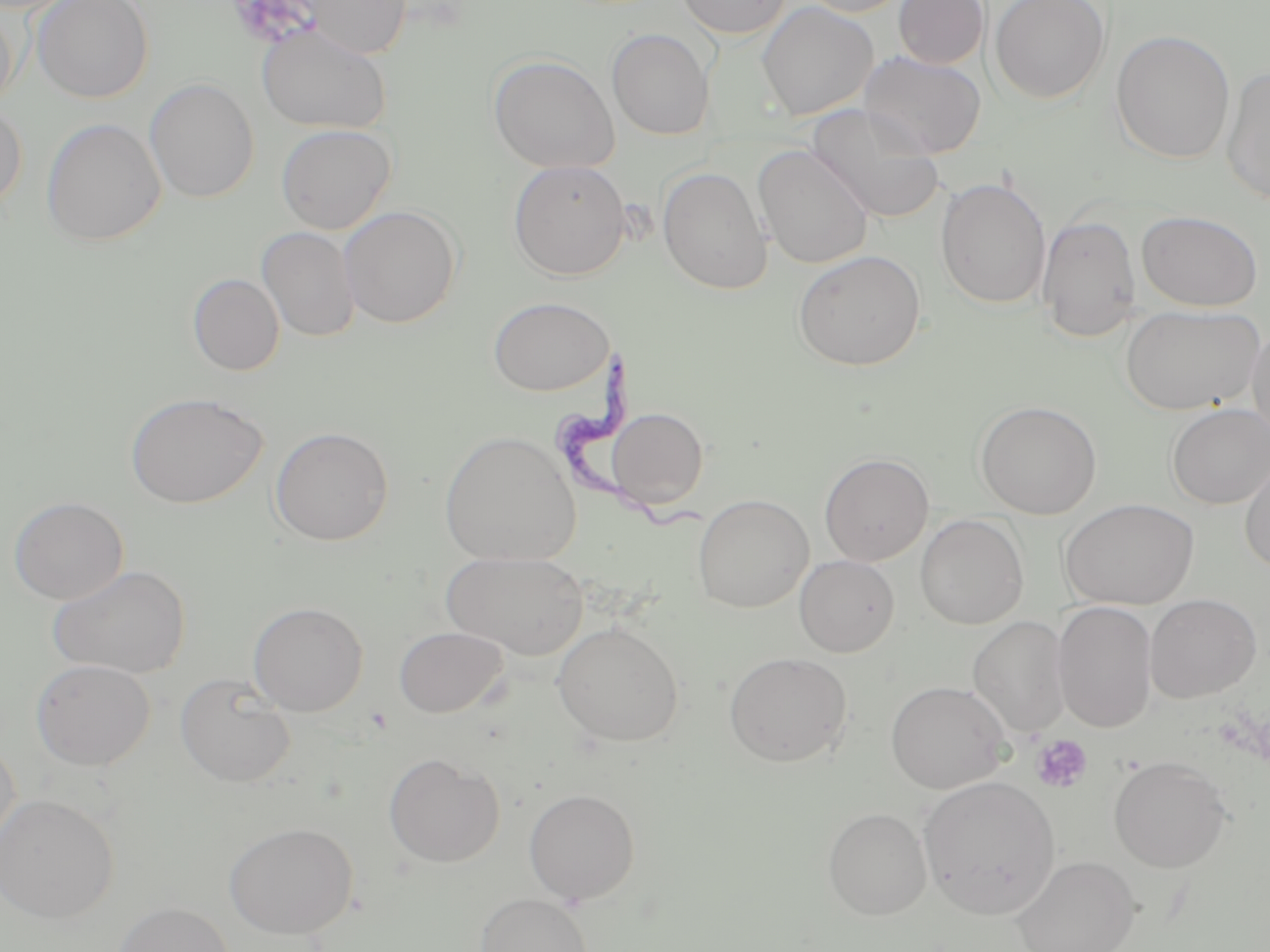
slide-level diagnosis = Trypanosoma brucei
field of view = one of a larger specimen
platelet locations = approximate bounding boxes as (x1, y1, x2, y2) in pixels: (223, 1, 320, 49), (1030, 734, 1093, 793)
image size = 1270×952 pixels
preparation = thin blood smear
stain = May-Grünwald-Giemsa
magnification = 1000x
modality = optical microscopy
Trypanosoma brucei locations = approximate bounding boxes as (x1, y1, x2, y2) in pixels: (555, 350, 704, 530)
uninfected red blood cell locations = approximate bounding boxes as (x1, y1, x2, y2) in pixels: (33, 0, 154, 103), (297, 0, 412, 59), (674, 0, 791, 39), (794, 0, 913, 17), (893, 0, 988, 69), (989, 0, 1111, 104), (756, 2, 878, 120), (0, 4, 19, 113), (257, 24, 390, 134), (607, 28, 715, 140), (1111, 29, 1235, 164), (857, 51, 987, 159), (488, 54, 619, 174), (1221, 67, 1270, 206), (144, 78, 259, 203), (0, 100, 28, 216), (808, 107, 945, 223), (41, 117, 166, 247), (275, 123, 396, 234), (752, 144, 874, 269), (508, 160, 631, 280), (657, 166, 773, 295), (935, 176, 1051, 310), (339, 205, 461, 328), (1137, 210, 1264, 311), (1037, 214, 1142, 342), (257, 226, 360, 342), (793, 250, 926, 371), (187, 273, 285, 376), (487, 296, 614, 396), (1120, 304, 1264, 415), (1247, 322, 1270, 447), (125, 392, 268, 509), (975, 400, 1102, 519), (1166, 403, 1270, 509), (606, 407, 709, 510), (270, 426, 394, 546), (439, 429, 581, 567), (1239, 451, 1270, 576), (819, 453, 934, 565), (692, 493, 814, 613), (9, 496, 129, 604), (1058, 498, 1200, 610), (915, 514, 1029, 630), (442, 550, 589, 659), (794, 555, 899, 657), (48, 564, 191, 679), (1145, 594, 1262, 703), (248, 601, 368, 716), (1053, 602, 1158, 733), (968, 615, 1069, 737), (552, 622, 684, 747), (394, 626, 508, 718), (724, 651, 853, 767), (30, 659, 156, 770), (175, 674, 296, 788), (886, 680, 1010, 794), (0, 737, 20, 863), (384, 753, 505, 868), (1108, 755, 1232, 873), (918, 775, 1060, 920), (524, 788, 641, 904), (0, 793, 119, 922), (822, 806, 932, 920), (224, 822, 358, 939), (1010, 854, 1140, 952), (475, 893, 593, 952), (111, 901, 236, 952)